Report the malaria status of this cell.
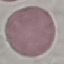
Uninfected.

Giemsa stain. Cell patch, automatically extracted from a larger field of view and resized to 64 × 64 pixels. Thin blood smear. Photographed with a smartphone camera at the microscope eyepiece.